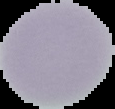 The area outside the segmented cell region is set to black. From a thin blood smear. Image is 115×109 pixels. Result: no malaria parasites detected.